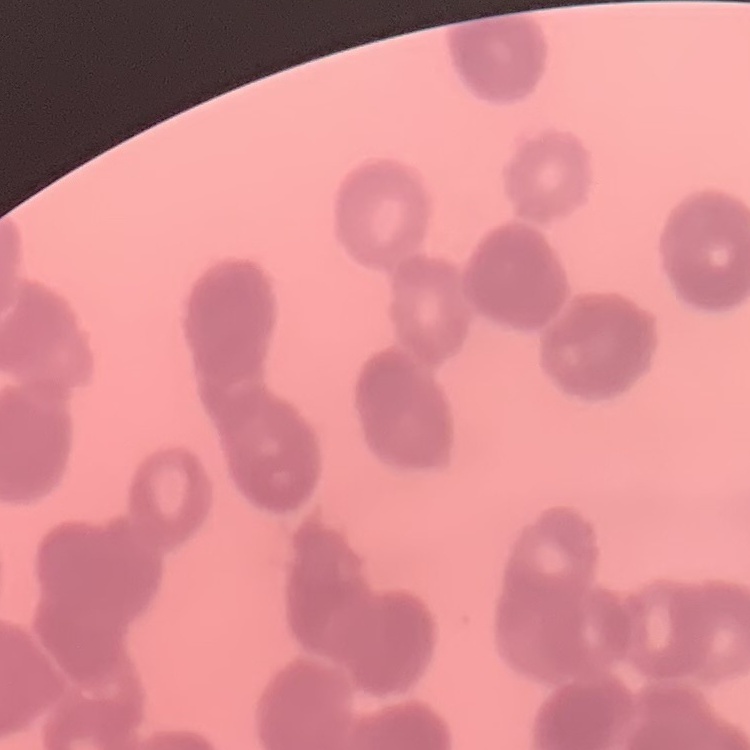
Summary:
  - Red blood cell morphology: rouleaux formation
  - Image type: one tile cut from a larger photomicrograph
  - Stain: Field's or Giemsa
  - Preparation: thin blood film